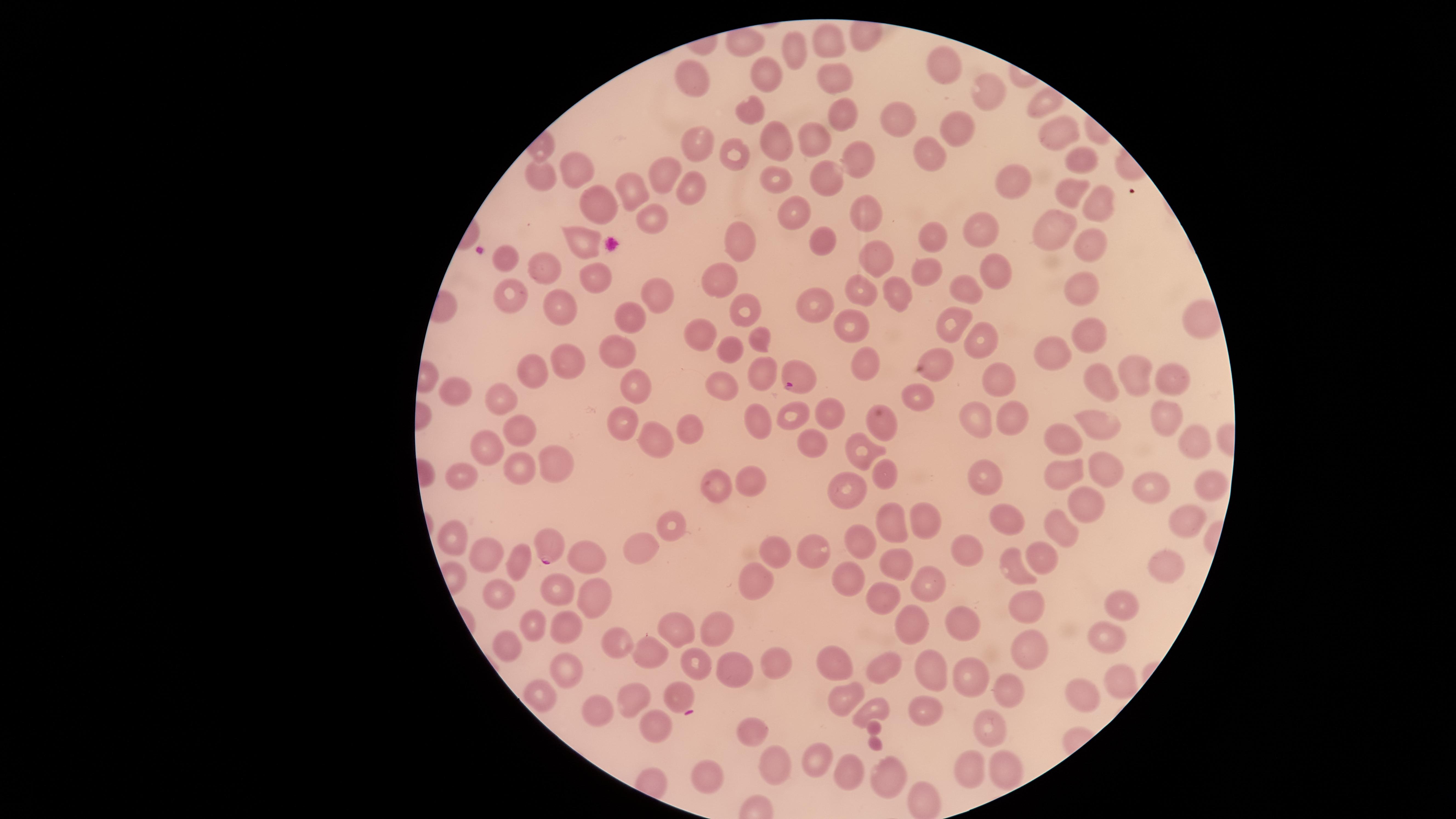
Approximate marker points as [x, y] in pixels.
Summary:
  - Parasitized red blood cells: [796, 381], [547, 542]
  - Uninfected red blood cells: [830, 40], [795, 45], [942, 60], [766, 70], [834, 75], [691, 81], [989, 92], [1044, 106], [747, 107], [843, 117], [894, 119], [957, 131], [1051, 132], [815, 137], [775, 140], [697, 145], [734, 152], [930, 155], [1080, 157], [854, 161], [576, 168], [665, 173], [547, 175], [825, 177], [1018, 179], [775, 180], [629, 188], [692, 188], [1071, 192], [1094, 200], [600, 207], [790, 211], [862, 215], [653, 223], [981, 231], [1044, 231], [1091, 238], [736, 240], [937, 240], [823, 242], [581, 244], [874, 257], [503, 258], [548, 268], [996, 268], [926, 273], [598, 278], [718, 281], [964, 287], [1082, 287], [504, 289], [894, 291], [651, 292], [863, 292], [562, 305], [814, 306], [744, 310], [632, 320], [1201, 320], [848, 324], [951, 324], [700, 332], [758, 339], [977, 339], [1098, 339], [729, 347], [615, 352], [1049, 354], [934, 358], [569, 361], [864, 361], [761, 371], [1134, 371], [534, 372], [1001, 377], [1162, 377], [1105, 382], [636, 385], [455, 391], [503, 392], [725, 392], [915, 397], [827, 410], [791, 414], [1011, 415], [1167, 416], [756, 421], [884, 422], [976, 422], [624, 424], [690, 424], [1096, 426], [518, 427], [1193, 436], [657, 438], [1064, 438], [486, 444], [814, 444], [863, 454], [555, 464], [1100, 467], [519, 469], [1062, 470], [889, 473], [461, 475], [988, 475], [1208, 480], [755, 481], [714, 485], [1146, 487], [847, 492], [1086, 507], [1008, 515], [933, 517], [1188, 522], [672, 526], [892, 526], [1057, 532], [452, 537], [863, 542], [772, 546], [639, 550], [813, 550], [966, 550], [485, 553], [584, 558], [1043, 560], [514, 564], [895, 566], [1164, 567], [1016, 570], [756, 580], [849, 581], [926, 581], [558, 591], [495, 593], [879, 596], [591, 597], [1122, 602], [1026, 608], [912, 622], [564, 623], [534, 624], [962, 627], [676, 629], [716, 630], [1109, 638], [506, 640], [615, 642], [1026, 651], [648, 653], [830, 657], [698, 664], [775, 664], [933, 667], [885, 669], [569, 670], [732, 670], [971, 681], [1115, 681], [1009, 687], [543, 695], [676, 696], [626, 698], [842, 698], [1087, 700], [871, 711], [594, 712], [923, 712], [651, 726], [754, 729], [988, 731], [816, 765], [782, 768], [968, 768], [1008, 769], [848, 770], [710, 773], [882, 773]
  - Visible region: circular
  - Capture: smartphone photograph through the microscope eyepiece
  - Preparation: thin smear of blood
  - Species: Plasmodium falciparum
  - Field of view: single
  - Presence: malaria parasites detected
  - Stain: Giemsa
  - Image size: 1456×819 pixels